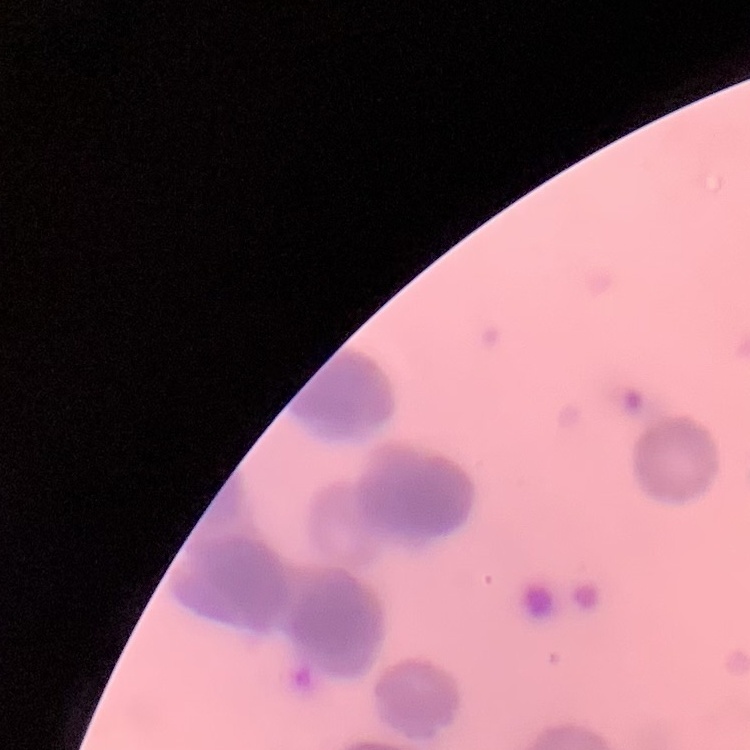

The erythrocytes exhibit rouleaux formation. Thin blood smear. One tile cut from a larger photomicrograph. Field's or Giemsa stain.